Assess this cell for malaria.
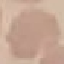

Uninfected.

Thin smear of blood. Photographed with a smartphone camera at the microscope eyepiece. Automatically extracted cell patch, resized to 64 × 64 pixels. Giemsa-stained preparation.